Comment on the morphology of the red blood cells.
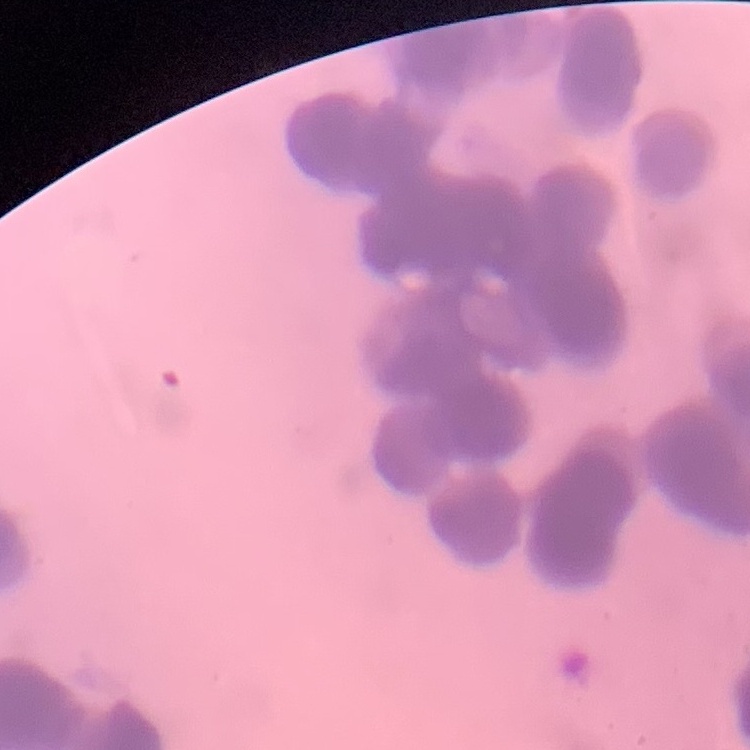
They show rouleaux formation.

Stained with either Field's or Giemsa. Square crop of a larger photomicrograph. Thin peripheral smear.